State which parasite is depicted.
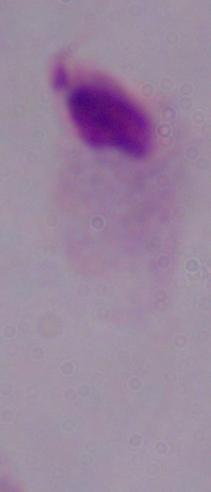
A trichomonad.

Micrograph. Captured at 1000x magnification.